Locate and identify every blood parasite.
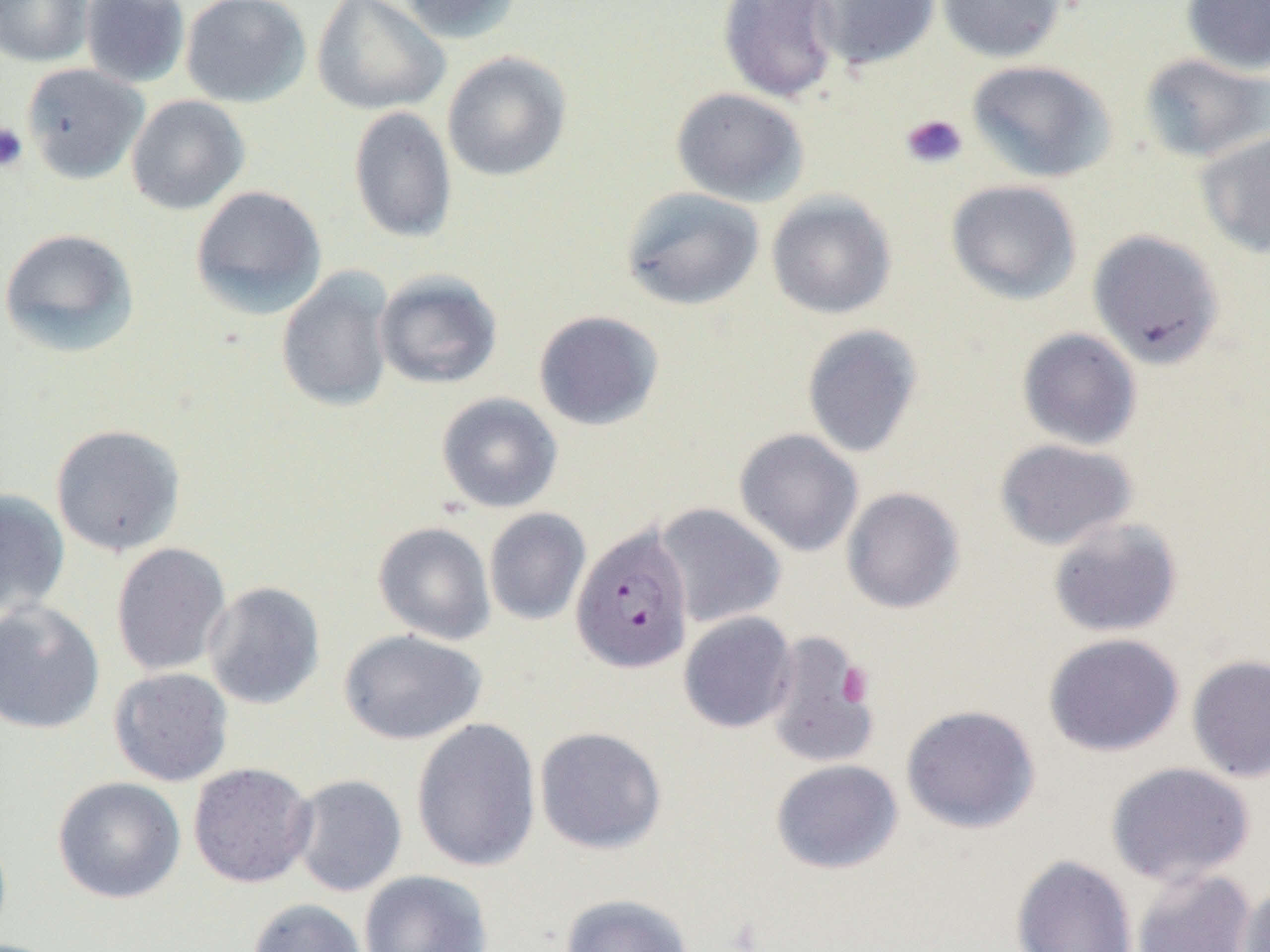

Approximate bounding boxes as (x1,y1)-(x2,y2) corner pairs in pixels.
Plasmodium falciparum-infected red blood cells: (571,524)-(694,675).
No Plasmodium ovale, Plasmodium malariae, Plasmodium vivax, Babesia divergens, or Trypanosoma brucei observed.

slide-level diagnosis = Plasmodium falciparum
preparation = thin blood smear
uninfected red blood cell locations = approximate bounding boxes as (x1,y1)-(x2,y2) corner pairs in pixels: (1,0)-(93,66), (80,0)-(190,88), (181,0)-(311,108), (312,0)-(450,116), (398,0)-(523,44), (717,0)-(843,104), (811,0)-(940,70), (937,0)-(1067,63), (1181,0)-(1270,75), (441,50)-(572,182), (1139,53)-(1270,164), (966,60)-(1116,183), (22,63)-(149,184), (670,86)-(809,207), (126,95)-(250,215), (348,106)-(457,244), (1196,130)-(1270,258), (945,179)-(1082,305), (190,185)-(327,319), (620,186)-(764,311), (766,190)-(897,320), (0,228)-(140,358), (1087,229)-(1225,369), (276,267)-(396,413), (374,269)-(503,390), (533,309)-(665,431), (801,324)-(924,458), (1017,328)-(1142,450), (436,392)-(563,513), (50,423)-(186,557), (734,428)-(864,557), (994,438)-(1139,551), (841,487)-(964,614), (0,489)-(70,618), (654,503)-(786,628), (484,508)-(591,626), (1047,517)-(1182,638), (373,521)-(496,645), (110,542)-(231,677), (203,581)-(325,710), (0,600)-(105,734), (678,611)-(797,733), (339,629)-(487,745), (763,630)-(880,769), (1043,633)-(1184,757), (1186,654)-(1270,782), (108,667)-(234,786), (900,704)-(1041,834), (411,717)-(541,872), (534,726)-(667,855), (770,759)-(903,874), (188,762)-(317,888), (1106,762)-(1255,887), (290,774)-(408,897), (52,776)-(186,904), (1010,854)-(1139,952), (1130,868)-(1258,952), (359,869)-(493,952), (1237,883)-(1270,952), (558,893)-(696,952), (247,897)-(369,952)
magnification = 1000x
modality = light microscopy
field of view = one of a larger specimen
platelet locations = approximate bounding boxes as (x1,y1)-(x2,y2) corner pairs in pixels: (900,113)-(968,170), (0,122)-(29,173), (837,663)-(874,706)
image size = 1270×952 pixels